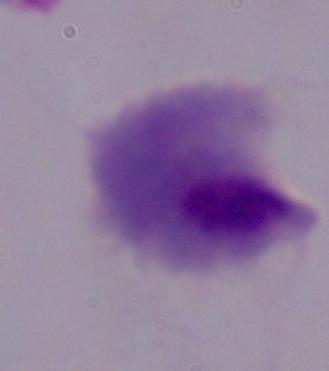
identification = trichomonad
modality = micrograph
magnification = 1000x